Classify this cell by malaria status.
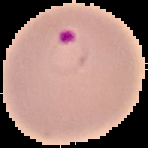

It is parasitized.

Summary:
  - Preparation: thin blood film
  - Image size: 148×148 pixels
  - Image type: segmented cell region with the area outside set to black